Locate every blood parasite and identify its species.
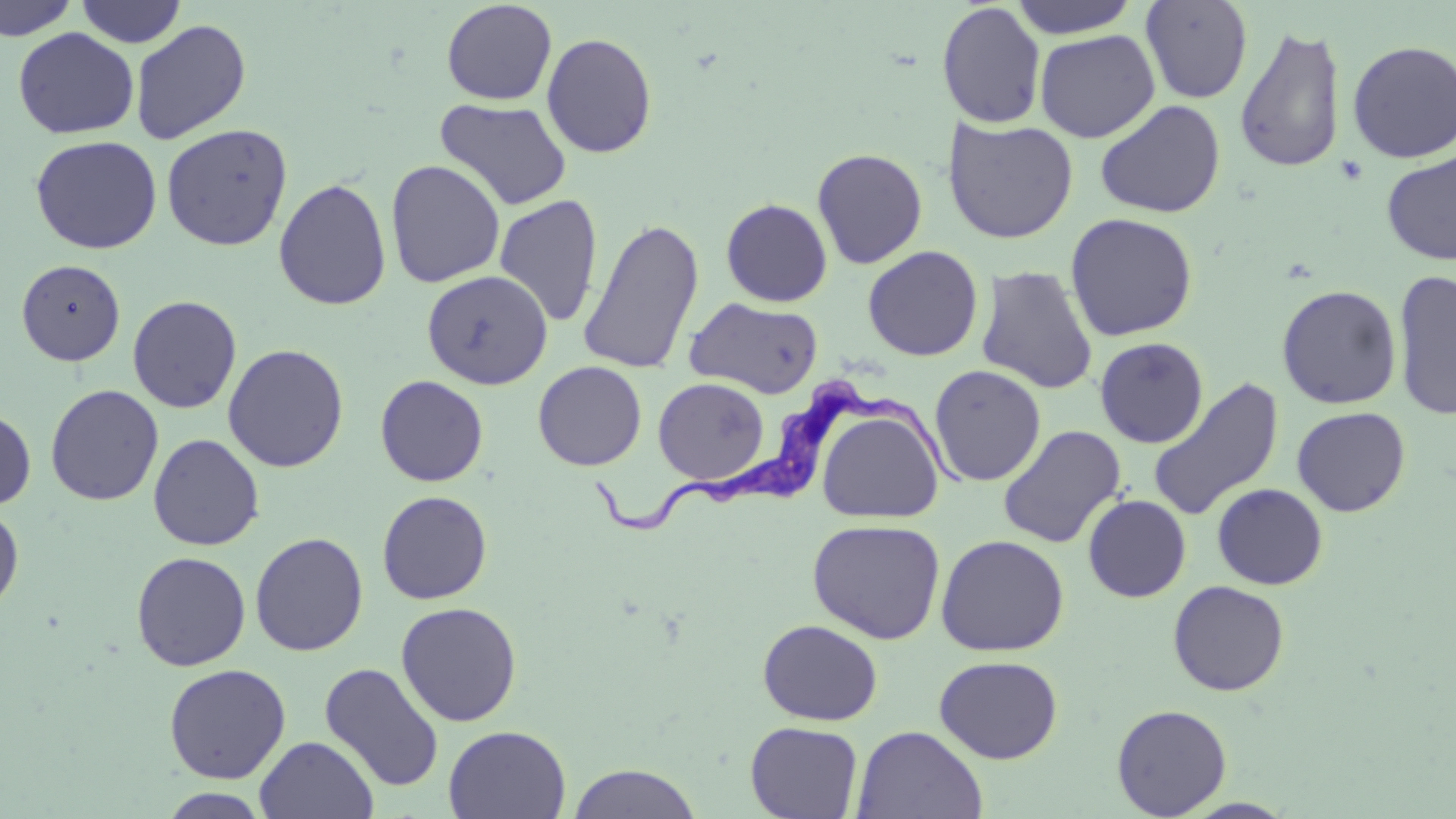
Approximate bounding boxes as named x1/y1/x2/y2 corners in pixels.
Trypanosoma brucei: (x1=589, y1=378, x2=974, y2=533).
No Plasmodium falciparum, Plasmodium ovale, Plasmodium malariae, Plasmodium vivax, or Babesia divergens observed.

slide-level diagnosis = Trypanosoma brucei
preparation = thin blood film
stain = May-Grünwald-Giemsa
modality = light microscopy
magnification = 1000x
image size = 1456×819 pixels
uninfected red blood cell locations = approximate bounding boxes as named x1/y1/x2/y2 corners in pixels: (x1=0, y1=0, x2=79, y2=41), (x1=75, y1=0, x2=187, y2=47), (x1=1009, y1=0, x2=1140, y2=38), (x1=1140, y1=0, x2=1253, y2=104), (x1=441, y1=1, x2=557, y2=105), (x1=936, y1=2, x2=1047, y2=129), (x1=130, y1=20, x2=251, y2=145), (x1=1233, y1=23, x2=1347, y2=175), (x1=14, y1=28, x2=139, y2=139), (x1=1034, y1=29, x2=1159, y2=142), (x1=541, y1=32, x2=658, y2=158), (x1=1347, y1=40, x2=1456, y2=163), (x1=435, y1=98, x2=572, y2=211), (x1=1082, y1=98, x2=1209, y2=339), (x1=1094, y1=99, x2=1226, y2=218), (x1=942, y1=117, x2=1079, y2=244), (x1=161, y1=123, x2=292, y2=251), (x1=417, y1=131, x2=540, y2=267), (x1=30, y1=135, x2=162, y2=253), (x1=812, y1=148, x2=928, y2=269), (x1=1381, y1=151, x2=1456, y2=265), (x1=385, y1=159, x2=506, y2=288), (x1=273, y1=177, x2=391, y2=311), (x1=494, y1=194, x2=604, y2=327), (x1=720, y1=198, x2=833, y2=307), (x1=1065, y1=212, x2=1198, y2=342), (x1=578, y1=217, x2=705, y2=375), (x1=862, y1=245, x2=984, y2=361), (x1=16, y1=259, x2=125, y2=366), (x1=976, y1=266, x2=1098, y2=394), (x1=421, y1=269, x2=553, y2=390), (x1=1392, y1=269, x2=1456, y2=421), (x1=1276, y1=284, x2=1402, y2=409), (x1=128, y1=295, x2=242, y2=413), (x1=685, y1=298, x2=824, y2=398), (x1=1094, y1=337, x2=1208, y2=448), (x1=223, y1=344, x2=349, y2=473), (x1=533, y1=361, x2=647, y2=471), (x1=928, y1=364, x2=1046, y2=487), (x1=375, y1=375, x2=489, y2=486), (x1=653, y1=378, x2=770, y2=484), (x1=1147, y1=378, x2=1284, y2=522), (x1=45, y1=385, x2=164, y2=506), (x1=1292, y1=406, x2=1411, y2=517), (x1=0, y1=407, x2=36, y2=511), (x1=818, y1=407, x2=943, y2=523), (x1=997, y1=425, x2=1126, y2=549), (x1=148, y1=433, x2=265, y2=551), (x1=1212, y1=483, x2=1328, y2=590), (x1=376, y1=490, x2=492, y2=604), (x1=1083, y1=495, x2=1191, y2=602), (x1=0, y1=504, x2=24, y2=614), (x1=807, y1=518, x2=946, y2=644), (x1=250, y1=532, x2=369, y2=657), (x1=935, y1=534, x2=1070, y2=656), (x1=131, y1=551, x2=251, y2=671), (x1=1167, y1=580, x2=1290, y2=696), (x1=395, y1=601, x2=522, y2=726), (x1=757, y1=619, x2=883, y2=726), (x1=934, y1=655, x2=1063, y2=764), (x1=319, y1=662, x2=444, y2=793), (x1=163, y1=663, x2=291, y2=784), (x1=1111, y1=703, x2=1232, y2=818), (x1=745, y1=721, x2=864, y2=818), (x1=443, y1=725, x2=571, y2=818), (x1=852, y1=726, x2=987, y2=819), (x1=255, y1=735, x2=378, y2=819), (x1=567, y1=763, x2=703, y2=819), (x1=158, y1=788, x2=272, y2=818), (x1=1177, y1=798, x2=1302, y2=818)
field of view = single